Assess this cell for malaria.
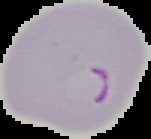
Parasitized.

preparation = thin blood film
image type = cell region segmented out of the field of view; surrounding area masked to black
image size = 151×139 pixels